Outline each blood parasite and name the species.
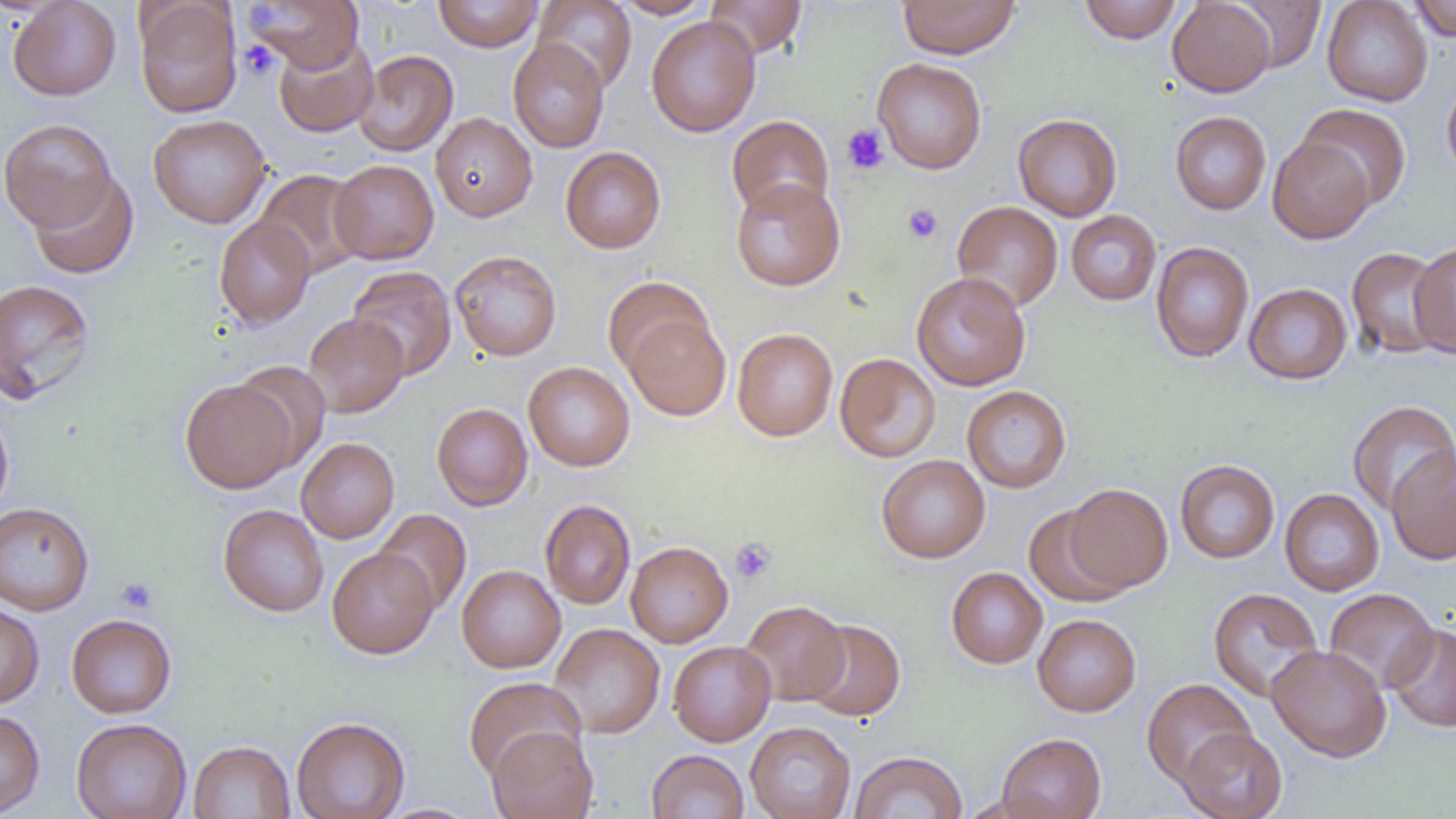
No blood parasites seen.

Approximate bounding boxes as [x1, y1, x2, y2] in pixels. Platelet locations: [239, 40, 280, 81], [841, 124, 890, 175], [902, 203, 943, 244], [730, 537, 777, 585], [115, 577, 158, 614]. Uninfected red blood cell locations: [8, 0, 122, 101], [245, 0, 364, 73], [433, 0, 543, 52], [612, 0, 714, 19], [705, 0, 807, 58], [896, 0, 1021, 58], [1079, 0, 1182, 43], [1167, 0, 1276, 97], [1227, 0, 1326, 73], [1322, 0, 1433, 107], [1409, 0, 1456, 41], [134, 1, 243, 118], [532, 1, 637, 92], [646, 16, 761, 137], [274, 35, 378, 137], [508, 39, 610, 153], [353, 49, 458, 157], [872, 57, 987, 174], [1441, 78, 1456, 181], [1296, 103, 1412, 211], [1170, 111, 1271, 215], [430, 112, 537, 221], [1013, 113, 1123, 221], [148, 114, 271, 228], [726, 115, 834, 219], [0, 117, 118, 231], [1268, 136, 1374, 244], [560, 146, 666, 253], [329, 159, 439, 264], [254, 169, 366, 279], [28, 172, 138, 279], [731, 178, 846, 291], [951, 200, 1063, 312], [1066, 210, 1161, 306], [214, 216, 315, 330], [1151, 241, 1254, 363], [1410, 242, 1456, 359], [1346, 247, 1449, 359], [450, 250, 562, 361], [347, 266, 457, 380], [911, 271, 1031, 391], [602, 275, 714, 377], [0, 277, 97, 405], [1244, 283, 1352, 384], [303, 312, 409, 417], [623, 314, 730, 421], [732, 327, 838, 441], [835, 353, 940, 462], [231, 361, 332, 471], [523, 361, 635, 471], [180, 379, 296, 493], [962, 385, 1071, 493], [1346, 400, 1456, 516], [0, 402, 14, 521], [431, 402, 533, 510], [296, 437, 399, 543], [1386, 444, 1456, 565], [876, 455, 990, 563], [1175, 459, 1279, 563], [1063, 483, 1173, 593], [1279, 488, 1384, 596], [540, 500, 635, 610], [0, 501, 94, 615], [1023, 503, 1130, 607], [218, 504, 329, 617], [373, 508, 472, 615], [625, 541, 733, 647], [326, 547, 438, 659], [456, 565, 565, 673], [946, 567, 1048, 669], [1208, 587, 1324, 702], [1324, 588, 1438, 694], [740, 600, 849, 706], [0, 601, 44, 709], [66, 613, 177, 718], [1033, 613, 1141, 717], [802, 618, 906, 721], [549, 623, 665, 739], [1385, 623, 1456, 733], [668, 641, 776, 746], [1266, 644, 1392, 762], [463, 676, 586, 782], [1141, 678, 1256, 788], [0, 709, 45, 817], [290, 716, 411, 818], [71, 718, 192, 819], [745, 721, 856, 819], [487, 726, 598, 819], [1177, 727, 1287, 819], [997, 732, 1106, 819], [188, 740, 294, 819], [646, 749, 749, 819], [849, 750, 967, 819]. Slide-level diagnosis: no evidence of blood parasites. Image is 1456×819 pixels. Thin blood smear. 1000x magnification. Optical microscopy. One field of a larger specimen.